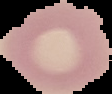
Summary:
  - Image type: segmented cell region with the area outside set to black
  - Preparation: thin blood smear
  - Malaria status: uninfected
  - Image size: 112×94 pixels